State which parasite is depicted.
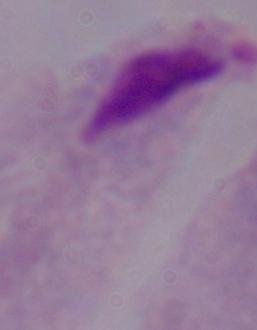

A trichomonad.

Micrograph. Captured at 1000x magnification.